Classify this cell by malaria status.
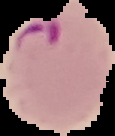

It is parasitized.

preparation = thin blood smear
image type = segmented cell region on a black background
image size = 115×136 pixels